Locate Plasmodium parasites and leukocytes.
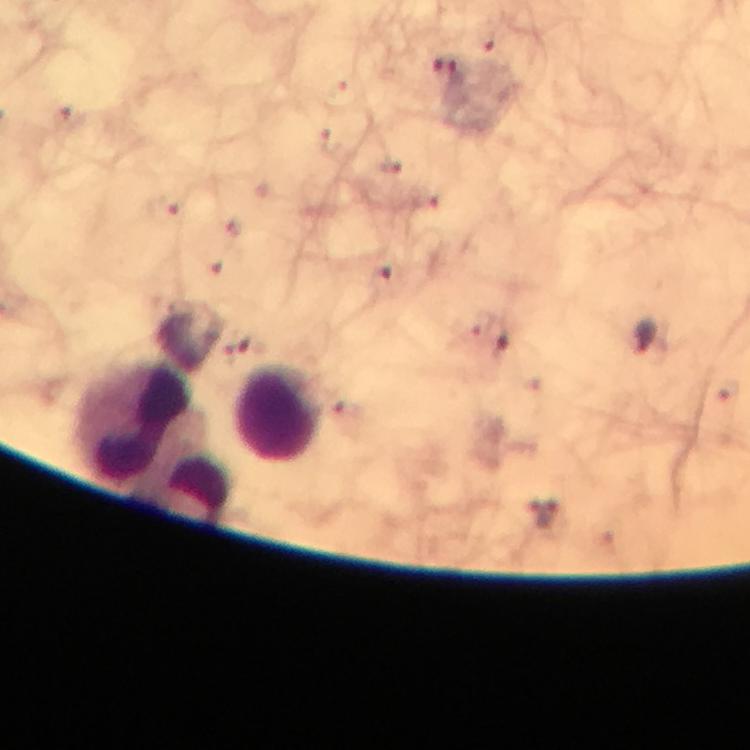

Approximate object centers, in pixels from the top-left corner.
Plasmodium parasites: (x=447, y=69), (x=69, y=114), (x=388, y=167), (x=164, y=209), (x=381, y=278), (x=493, y=336), (x=648, y=338).
Leukocytes: (x=280, y=414), (x=136, y=427), (x=197, y=493).

Summary:
  - Context: from a malaria diagnostic workup
  - Preparation: thick blood film
  - Image size: 750×750 pixels
  - Capture: smartphone mounted on the microscope
  - Magnification: 100x
  - Immersion oil: used
  - Cropped from: a single field of view
  - Stain: Giemsa